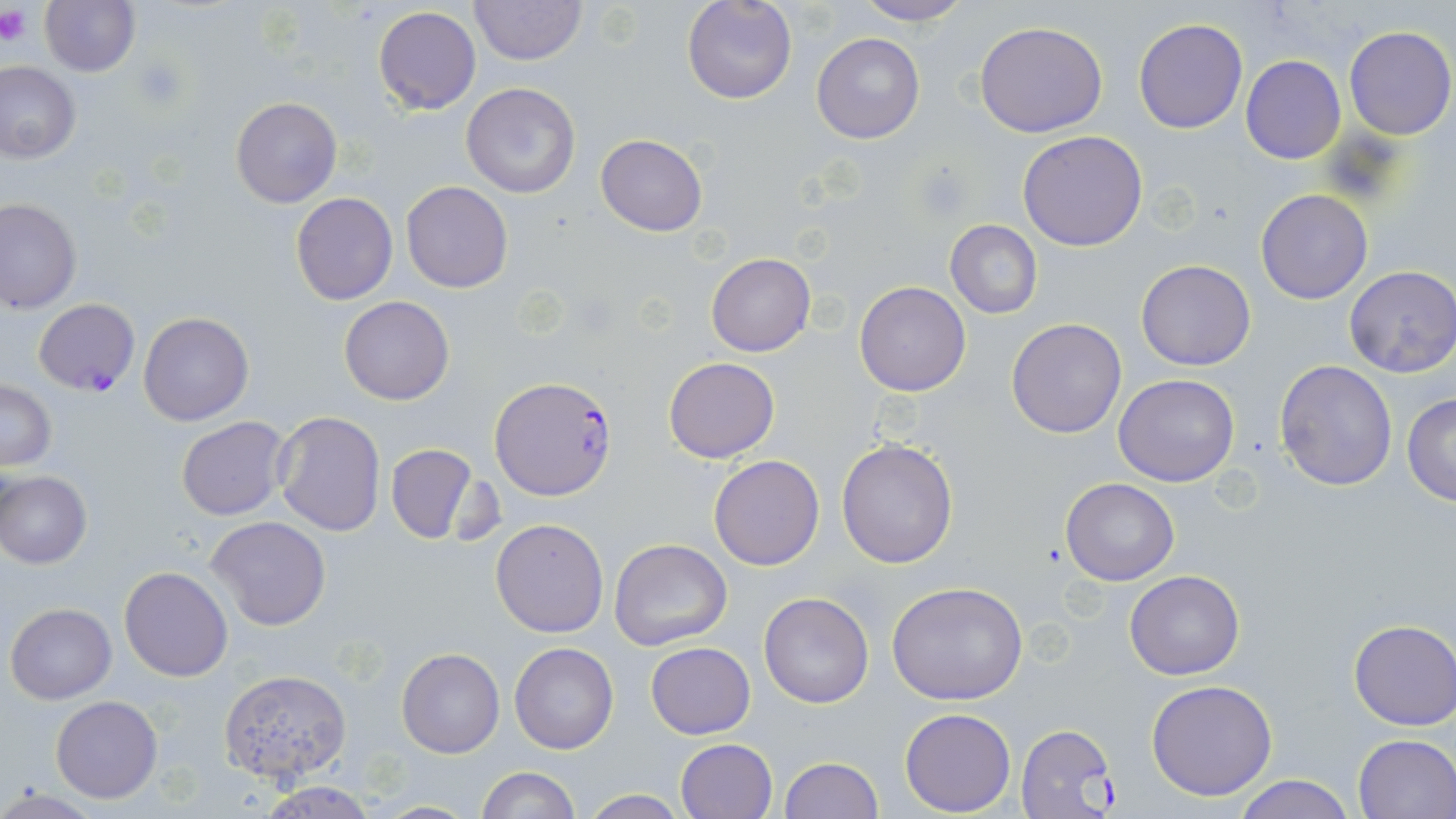 Approximate bounding boxes as named x1/y1/x2/y2 corners in pixels. Uninfected red blood cell locations: (x1=39, y1=0, x2=140, y2=77), (x1=469, y1=0, x2=585, y2=66), (x1=682, y1=0, x2=797, y2=104), (x1=854, y1=1, x2=973, y2=27), (x1=371, y1=6, x2=483, y2=114), (x1=1133, y1=18, x2=1248, y2=133), (x1=974, y1=21, x2=1108, y2=137), (x1=1343, y1=25, x2=1456, y2=139), (x1=811, y1=31, x2=926, y2=144), (x1=1240, y1=56, x2=1347, y2=165), (x1=0, y1=62, x2=81, y2=162), (x1=460, y1=83, x2=582, y2=199), (x1=231, y1=95, x2=342, y2=208), (x1=1018, y1=130, x2=1149, y2=251), (x1=595, y1=135, x2=707, y2=237), (x1=401, y1=181, x2=513, y2=294), (x1=1256, y1=189, x2=1373, y2=304), (x1=291, y1=192, x2=398, y2=305), (x1=0, y1=198, x2=81, y2=313), (x1=945, y1=220, x2=1043, y2=318), (x1=705, y1=253, x2=815, y2=356), (x1=1136, y1=259, x2=1257, y2=370), (x1=1345, y1=265, x2=1456, y2=377), (x1=855, y1=281, x2=970, y2=397), (x1=339, y1=296, x2=455, y2=405), (x1=138, y1=312, x2=253, y2=425), (x1=1007, y1=318, x2=1127, y2=439), (x1=664, y1=357, x2=780, y2=463), (x1=1275, y1=359, x2=1399, y2=491), (x1=1114, y1=374, x2=1240, y2=487), (x1=1, y1=379, x2=56, y2=471), (x1=1402, y1=392, x2=1456, y2=506), (x1=273, y1=411, x2=386, y2=538), (x1=175, y1=417, x2=290, y2=521), (x1=836, y1=438, x2=960, y2=569), (x1=384, y1=443, x2=482, y2=546), (x1=709, y1=456, x2=825, y2=571), (x1=0, y1=470, x2=92, y2=568), (x1=1060, y1=477, x2=1179, y2=586), (x1=205, y1=516, x2=332, y2=633), (x1=491, y1=517, x2=609, y2=638), (x1=610, y1=538, x2=732, y2=651), (x1=119, y1=566, x2=232, y2=681), (x1=1125, y1=569, x2=1244, y2=679), (x1=885, y1=580, x2=1029, y2=703), (x1=758, y1=591, x2=875, y2=709), (x1=5, y1=602, x2=116, y2=703), (x1=1347, y1=619, x2=1455, y2=732), (x1=646, y1=641, x2=755, y2=739), (x1=509, y1=642, x2=619, y2=754), (x1=397, y1=648, x2=504, y2=758), (x1=217, y1=668, x2=351, y2=785), (x1=1146, y1=679, x2=1277, y2=801), (x1=50, y1=696, x2=163, y2=803), (x1=899, y1=708, x2=1016, y2=815), (x1=1353, y1=734, x2=1456, y2=817), (x1=675, y1=738, x2=777, y2=819), (x1=780, y1=757, x2=884, y2=818), (x1=476, y1=766, x2=579, y2=819), (x1=1232, y1=774, x2=1357, y2=819), (x1=258, y1=782, x2=378, y2=818), (x1=580, y1=790, x2=690, y2=818), (x1=370, y1=801, x2=483, y2=817). Plasmodium falciparum-infected red blood cell locations: (x1=33, y1=296, x2=140, y2=397), (x1=493, y1=375, x2=617, y2=498), (x1=1014, y1=723, x2=1116, y2=818). Platelet locations: (x1=0, y1=5, x2=30, y2=47), (x1=134, y1=57, x2=185, y2=108). Slide-level diagnosis: Plasmodium falciparum. 1000x magnification. May-Grünwald-Giemsa stain. Single field of view. Thin blood smear. Light microscopy. Image is 1456×819 pixels.